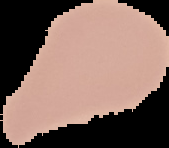

Result: no Plasmodium parasites seen. Image is 169×148 pixels. From a thin blood smear. Cell region segmented out of the field of view; the surrounding area is masked to black.